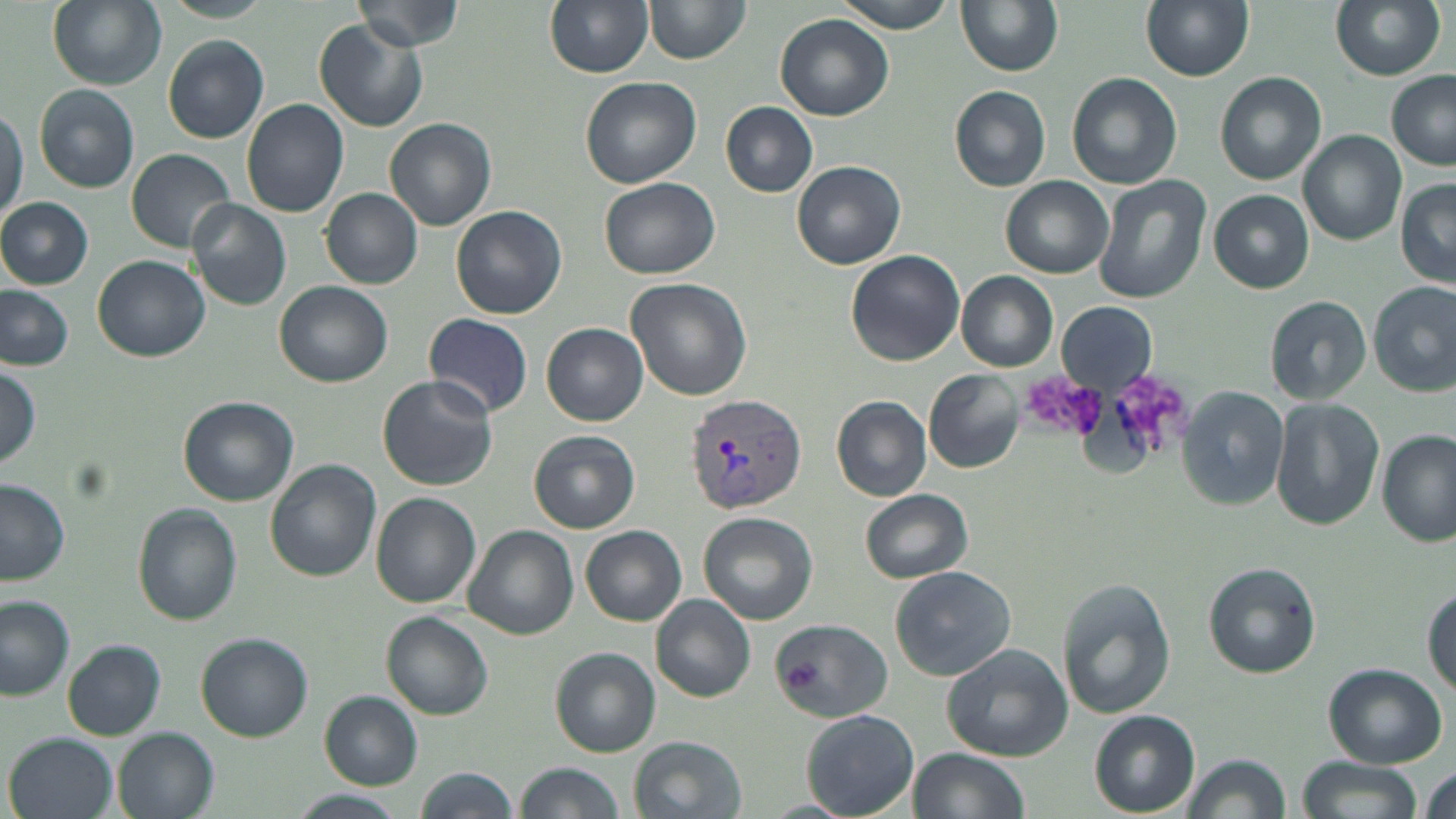
{
  "slide_level_diagnosis": "Plasmodium vivax",
  "magnification": "1000x",
  "image_size": "1456×819 pixels",
  "preparation": "thin blood smear",
  "stain": "May-Grünwald-Giemsa",
  "modality": "light microscopy",
  "plasmodium_vivax_infected_red_blood_cell_locations": "approximate bounding boxes as (x1, y1, x2, y2) in pixels: (686, 394, 808, 514)",
  "field_of_view": "one of a larger specimen",
  "uninfected_red_blood_cell_locations": "approximate bounding boxes as (x1, y1, x2, y2) in pixels: (46, 0, 166, 89), (158, 0, 275, 22), (354, 0, 463, 49), (544, 0, 653, 77), (830, 0, 959, 32), (955, 0, 1063, 76), (1140, 0, 1253, 80), (1330, 0, 1446, 80), (645, 2, 750, 65), (775, 14, 895, 121), (315, 21, 428, 132), (164, 37, 269, 143), (1215, 71, 1326, 184), (1066, 72, 1182, 189), (1384, 73, 1456, 172), (581, 75, 702, 187), (33, 84, 140, 193), (950, 86, 1051, 190), (241, 99, 348, 219), (721, 102, 819, 197), (0, 103, 27, 227), (386, 117, 495, 231), (1298, 130, 1406, 245), (127, 148, 239, 255), (793, 160, 904, 268), (1094, 175, 1211, 304), (1002, 176, 1112, 276), (599, 177, 722, 278), (1397, 180, 1456, 287), (321, 188, 422, 288), (1210, 189, 1314, 292), (0, 198, 93, 288), (185, 199, 292, 310), (450, 205, 568, 320), (845, 250, 965, 367), (93, 255, 210, 362), (956, 271, 1058, 371), (625, 276, 752, 402), (276, 280, 393, 385), (1369, 281, 1456, 396), (0, 285, 76, 370), (1265, 295, 1372, 404), (1057, 302, 1156, 392), (423, 312, 534, 419), (542, 323, 649, 426), (0, 365, 43, 472), (925, 369, 1024, 473), (378, 375, 499, 492), (1179, 388, 1289, 509), (179, 395, 299, 506), (831, 395, 932, 503), (1271, 398, 1385, 530), (528, 430, 640, 533), (1377, 430, 1455, 547), (266, 460, 381, 580), (0, 480, 71, 585), (859, 489, 973, 583), (371, 494, 481, 607), (133, 506, 242, 624), (698, 510, 818, 624), (463, 525, 578, 639), (581, 525, 686, 625), (1203, 562, 1320, 677), (889, 565, 1017, 680), (1057, 581, 1174, 719), (1423, 586, 1455, 695), (651, 595, 756, 703), (0, 598, 75, 698), (382, 611, 495, 718), (767, 619, 893, 720), (197, 633, 313, 741), (63, 640, 166, 739), (942, 644, 1072, 761), (550, 648, 661, 757), (1323, 663, 1447, 767), (319, 691, 422, 788), (801, 709, 919, 817), (1089, 710, 1200, 817), (114, 728, 219, 819), (7, 733, 118, 819), (629, 734, 749, 819), (907, 748, 1029, 819), (1182, 752, 1290, 819), (1295, 755, 1424, 819), (517, 761, 626, 818), (1421, 764, 1455, 819), (412, 767, 517, 819), (291, 791, 407, 819), (762, 799, 852, 817)"
}